Report the malaria status of this cell.
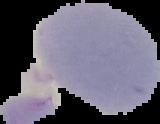
It is uninfected.

Summary:
  - Image size: 160×124 pixels
  - Preparation: thin blood film
  - Image type: segmented cell region with the area outside set to black